Name the parasite shown.
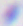

This is Toxoplasma gondii.

magnification = 400x
modality = micrograph